Locate platelets.
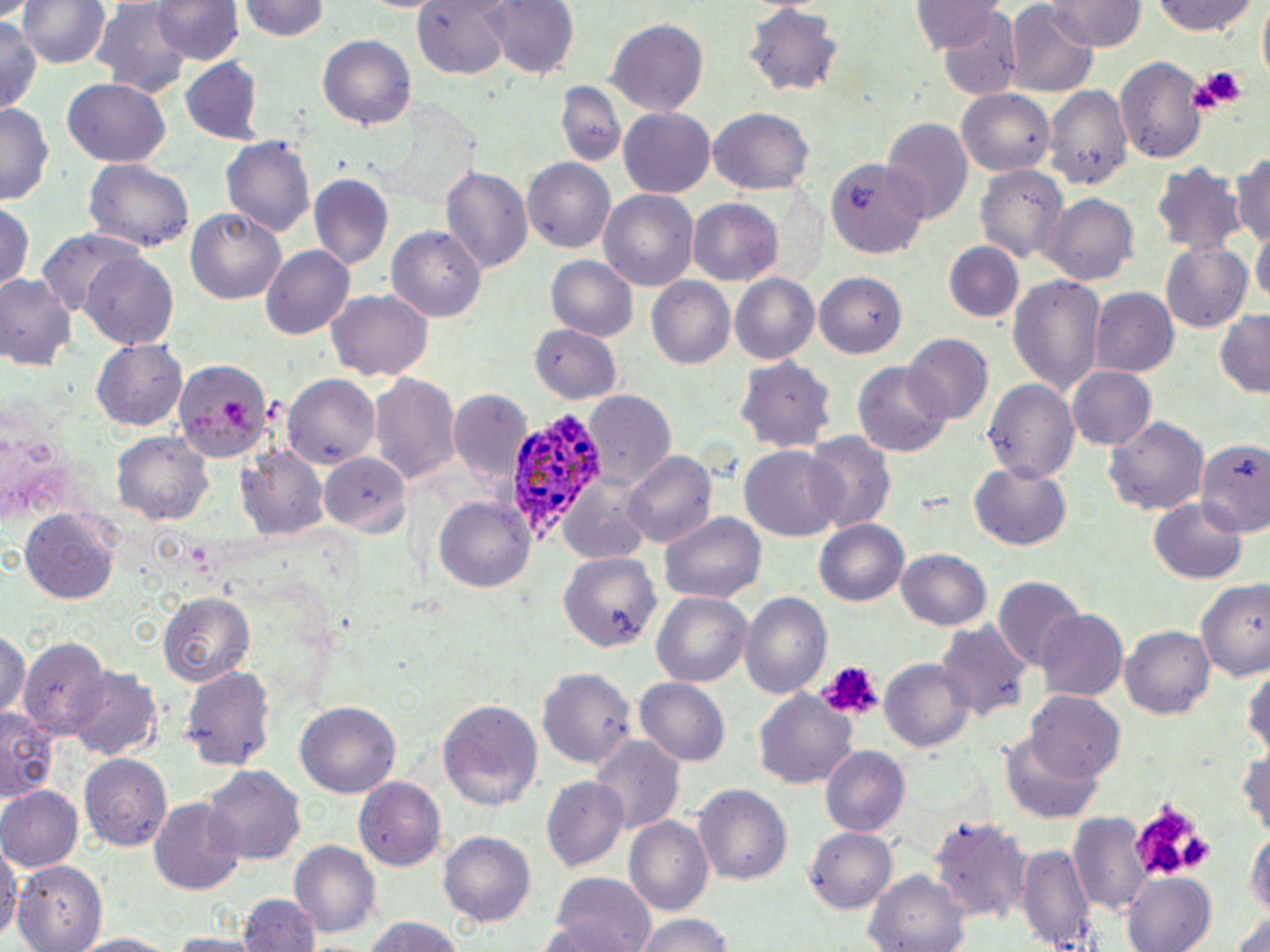

Approximate bounding boxes as [x1, y1, x2, y2] in pixels.
Platelets: [1185, 64, 1245, 113], [814, 659, 882, 724], [1131, 798, 1216, 880].

slide-level diagnosis = Plasmodium ovale
stain = May-Grünwald-Giemsa
uninfected red blood cell locations = approximate bounding boxes as [x1, y1, x2, y2] in pixels: [17, 0, 111, 70], [483, 0, 579, 79], [1047, 0, 1143, 50], [1147, 0, 1259, 38], [1255, 0, 1269, 88], [153, 1, 242, 65], [237, 1, 331, 43], [911, 2, 1004, 54], [1008, 2, 1098, 94], [91, 4, 194, 97], [742, 5, 844, 96], [932, 9, 1023, 98], [0, 12, 41, 117], [607, 17, 708, 115], [318, 38, 415, 128], [181, 60, 262, 142], [1116, 60, 1208, 162], [62, 79, 171, 166], [556, 81, 627, 168], [1045, 85, 1132, 190], [958, 90, 1054, 176], [0, 104, 52, 205], [618, 107, 716, 198], [703, 107, 815, 196], [882, 118, 973, 226], [223, 135, 316, 240], [1233, 147, 1270, 253], [521, 158, 616, 252], [828, 160, 928, 259], [84, 161, 193, 250], [1150, 161, 1246, 258], [973, 162, 1068, 265], [439, 165, 532, 276], [309, 173, 395, 270], [598, 189, 700, 293], [1040, 194, 1139, 283], [0, 199, 33, 291], [687, 199, 783, 286], [185, 208, 286, 305], [1253, 225, 1269, 313], [387, 226, 487, 322], [37, 228, 143, 317], [945, 240, 1023, 322], [1159, 242, 1255, 332], [261, 246, 356, 340], [81, 253, 180, 348], [546, 256, 639, 342], [814, 270, 906, 357], [730, 273, 819, 366], [0, 274, 79, 372], [1007, 274, 1104, 398], [645, 278, 736, 370], [1089, 287, 1178, 376], [327, 290, 431, 380], [1215, 308, 1270, 396], [530, 322, 624, 404], [902, 334, 992, 425], [92, 339, 188, 431], [737, 356, 834, 452], [172, 358, 271, 464], [851, 360, 953, 457], [1068, 366, 1158, 451], [284, 374, 381, 468], [367, 374, 459, 487], [982, 378, 1080, 483], [446, 386, 529, 487], [584, 393, 675, 490], [1105, 414, 1210, 515], [112, 431, 214, 524], [804, 431, 894, 534], [1194, 434, 1270, 536], [740, 447, 846, 540], [238, 448, 327, 539], [622, 449, 718, 551], [320, 454, 411, 537], [968, 461, 1072, 551], [558, 478, 657, 563], [433, 496, 535, 595], [1150, 499, 1249, 585], [19, 508, 121, 604], [661, 510, 767, 606], [814, 518, 909, 607], [897, 548, 993, 633], [559, 550, 662, 655], [1198, 577, 1269, 680], [993, 579, 1084, 674], [652, 591, 752, 689], [158, 592, 254, 687], [738, 592, 833, 704], [1036, 610, 1127, 699], [933, 623, 1033, 726], [1121, 626, 1214, 722], [0, 630, 29, 721], [20, 637, 111, 739], [881, 658, 973, 755], [1242, 659, 1270, 761], [181, 662, 278, 772], [538, 667, 637, 771], [68, 669, 163, 759], [636, 676, 733, 768], [754, 691, 857, 790], [1026, 692, 1125, 784], [437, 696, 542, 810], [294, 701, 402, 798], [0, 709, 55, 802], [1001, 731, 1105, 821], [592, 736, 683, 836], [1239, 736, 1270, 841], [820, 745, 909, 836], [83, 752, 174, 853], [202, 765, 306, 866], [356, 777, 446, 869], [542, 777, 630, 873], [693, 782, 792, 888], [0, 785, 82, 871], [148, 797, 247, 894], [1070, 812, 1152, 918], [930, 813, 1032, 925], [624, 817, 714, 919], [1245, 827, 1269, 916], [805, 828, 897, 915], [439, 832, 535, 929], [291, 840, 379, 937], [1019, 841, 1094, 952], [0, 843, 18, 948], [17, 862, 105, 952], [864, 869, 971, 952], [1123, 871, 1217, 952], [548, 873, 656, 952], [239, 892, 320, 952], [1227, 908, 1270, 952], [632, 914, 734, 952], [357, 915, 471, 952], [67, 932, 182, 952]
image size = 1270×952 pixels
Plasmodium ovale-infected red blood cell locations = approximate bounding boxes as [x1, y1, x2, y2] in pixels: [504, 410, 605, 537]
field of view = one of a larger specimen
preparation = thin blood smear
modality = light microscopy
magnification = 1000x